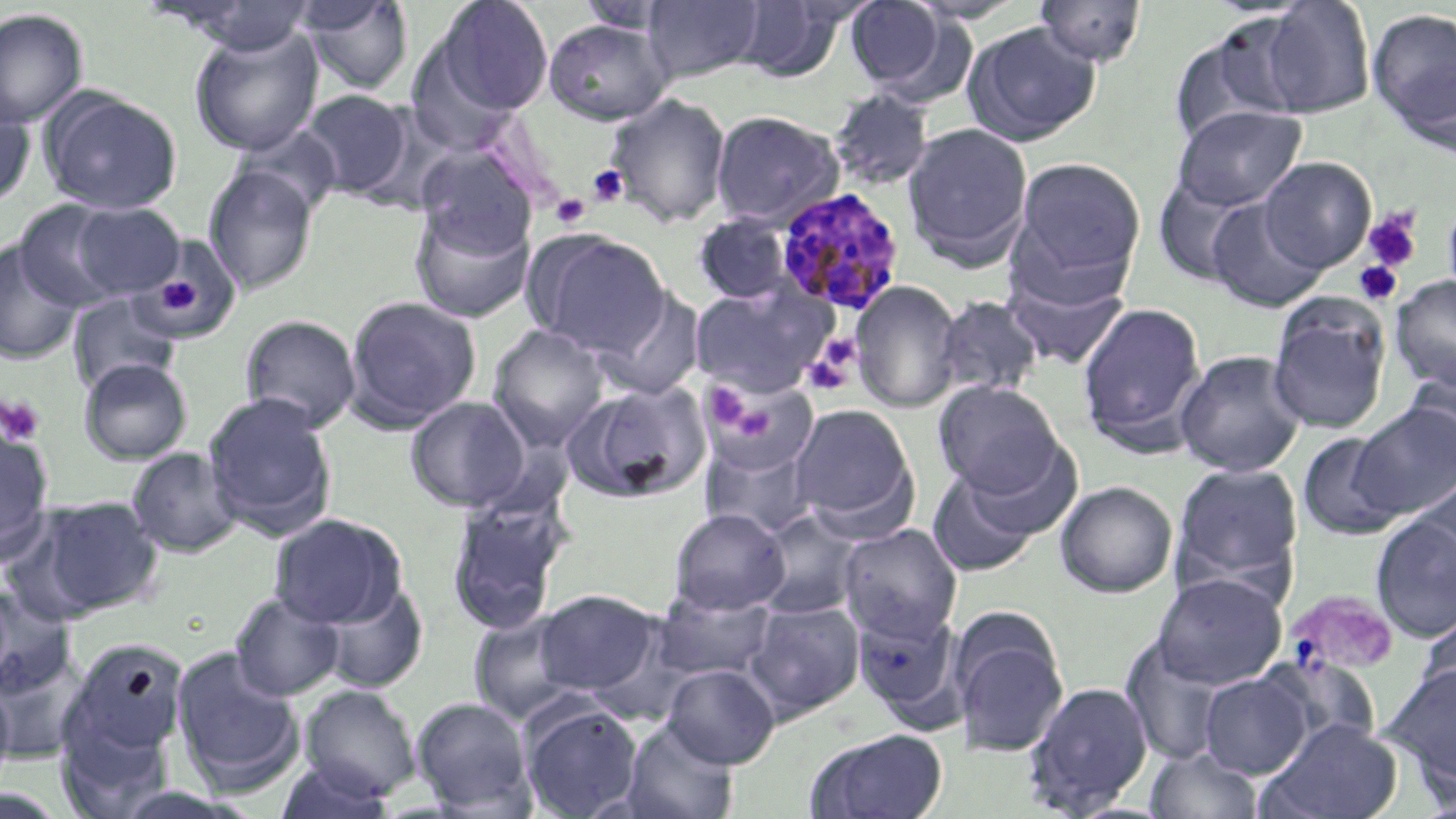
Summary:
  - Coordinate format: approximate bounding boxes as (x1, y1, x2, y2) in pixels
  - Platelet locations: (587, 165, 629, 207), (550, 194, 591, 228), (1362, 209, 1422, 273), (1353, 260, 1402, 305), (150, 264, 216, 322), (806, 334, 862, 391), (708, 385, 749, 426), (0, 394, 46, 445), (736, 407, 775, 440), (1307, 590, 1400, 667)
  - Plasmodium malariae-infected red blood cell locations: (775, 187, 906, 316)
  - Uninfected red blood cell locations: (296, 0, 414, 97), (642, 0, 766, 83), (843, 0, 962, 96), (160, 1, 321, 55), (433, 1, 554, 118), (575, 1, 678, 33), (731, 1, 848, 81), (1031, 1, 1149, 68), (1251, 1, 1376, 119), (0, 8, 88, 128), (1367, 9, 1456, 137), (544, 19, 673, 125), (1168, 20, 1307, 147), (962, 22, 1101, 146), (189, 25, 324, 156), (829, 88, 935, 191), (42, 90, 181, 214), (300, 90, 414, 200), (605, 93, 732, 227), (0, 95, 35, 210), (1173, 105, 1307, 211), (711, 109, 844, 229), (902, 121, 1034, 270), (416, 147, 537, 258), (1010, 155, 1147, 296), (1259, 157, 1376, 272), (203, 164, 319, 296), (1153, 176, 1259, 286), (1442, 195, 1456, 309), (1207, 197, 1327, 314), (13, 200, 132, 311), (409, 202, 535, 324), (71, 203, 185, 300), (694, 213, 795, 305), (525, 229, 670, 356), (142, 238, 240, 342), (0, 242, 84, 365), (1002, 263, 1131, 372), (1390, 275, 1456, 391), (850, 280, 962, 413), (689, 283, 835, 397), (592, 288, 706, 400), (66, 293, 181, 396), (344, 295, 482, 430), (933, 295, 1044, 400), (1266, 296, 1392, 435), (1076, 300, 1207, 454), (240, 314, 361, 433), (487, 324, 610, 449), (1175, 350, 1306, 476), (79, 358, 192, 465), (1402, 367, 1456, 475), (702, 377, 820, 479), (934, 381, 1065, 496), (564, 382, 711, 504), (202, 392, 338, 537), (405, 396, 531, 512), (789, 402, 919, 535), (1351, 403, 1455, 520), (0, 426, 54, 562), (1297, 431, 1406, 540), (699, 436, 819, 538), (953, 438, 1083, 545), (126, 447, 242, 558), (1170, 462, 1304, 594), (927, 469, 1041, 577), (1408, 474, 1456, 594), (1054, 481, 1177, 598), (445, 493, 569, 636), (19, 495, 164, 621), (668, 508, 791, 615), (754, 508, 864, 620), (1370, 512, 1456, 643), (268, 513, 406, 628), (838, 524, 962, 641), (1152, 573, 1287, 689), (314, 581, 427, 692), (0, 585, 76, 700), (532, 589, 662, 699), (652, 589, 778, 683), (230, 593, 346, 701), (744, 600, 864, 719), (853, 603, 965, 728), (1418, 606, 1456, 716), (468, 609, 589, 725), (949, 609, 1069, 757), (1120, 635, 1237, 766), (65, 637, 190, 758), (0, 644, 93, 763), (171, 646, 304, 793), (1259, 663, 1381, 755), (662, 664, 780, 768), (1379, 664, 1456, 786), (1199, 672, 1312, 779), (0, 680, 15, 802), (1022, 681, 1153, 816), (300, 685, 420, 799), (411, 696, 534, 815), (518, 699, 644, 819), (1263, 717, 1403, 818), (56, 718, 174, 817), (620, 718, 739, 819), (808, 728, 949, 819), (1144, 747, 1266, 819), (273, 758, 399, 819)
  - Slide-level diagnosis: Plasmodium malariae
  - Preparation: thin blood smear
  - Modality: light microscopy
  - Stain: May-Grünwald-Giemsa
  - Image size: 1456×819 pixels
  - Field of view: one of a larger specimen
  - Magnification: 1000x